Report the malaria status of this cell.
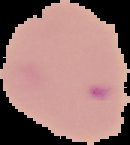

Parasitized.

From a thin blood smear. Segmented cell region on a black background. Image is 130×145 pixels.